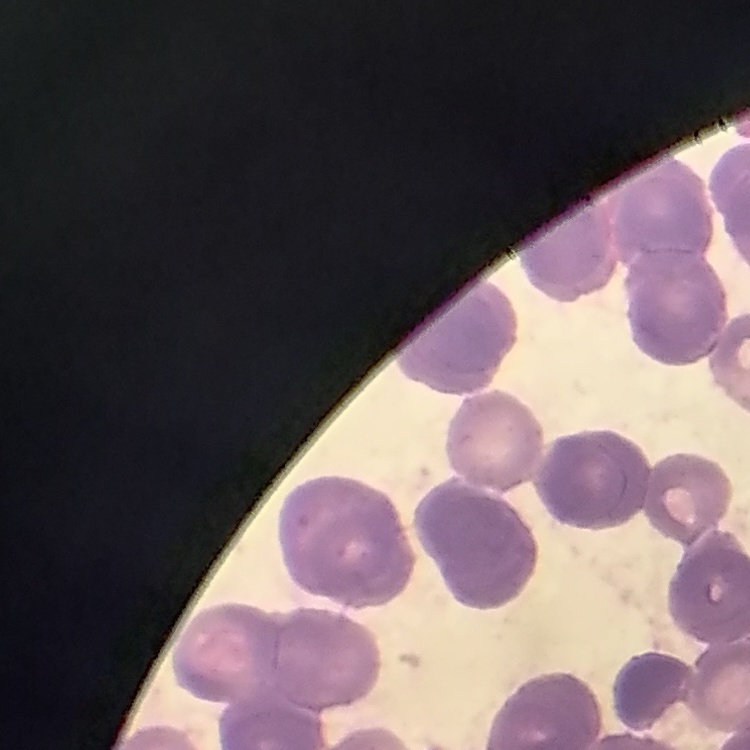 The erythrocytes show rouleaux formation. Field's or Giemsa stain. Thin blood smear. One tile cut from a larger photomicrograph.